Classify this cell by malaria status.
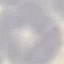

It is uninfected.

Giemsa stain. Automatically extracted cell patch, resized to 64 × 64 pixels. Thin smear of blood. Acquired by smartphone through the microscope eyepiece.